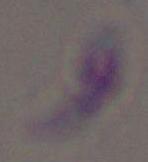

{
  "magnification": "1000x",
  "identification": "Toxoplasma gondii",
  "modality": "micrograph"
}